Assess this cell for malaria.
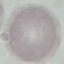
It is uninfected.

Summary:
  - Preparation: thin smear
  - Stain: Giemsa
  - Image type: cell patch, automatically extracted from a larger field of view and resized to 64 × 64 pixels
  - Capture: smartphone through the microscope eyepiece